State which parasite is depicted.
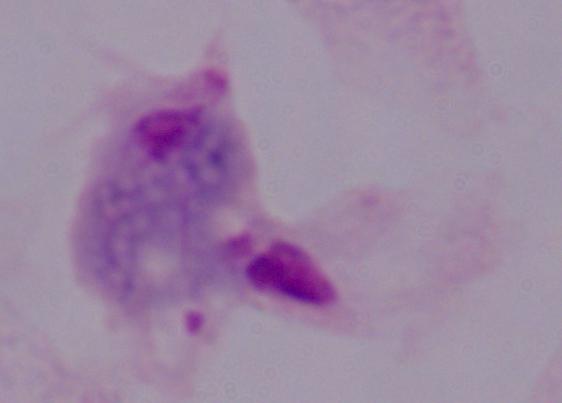
This is a trichomonad.

magnification = 1000x
modality = micrograph